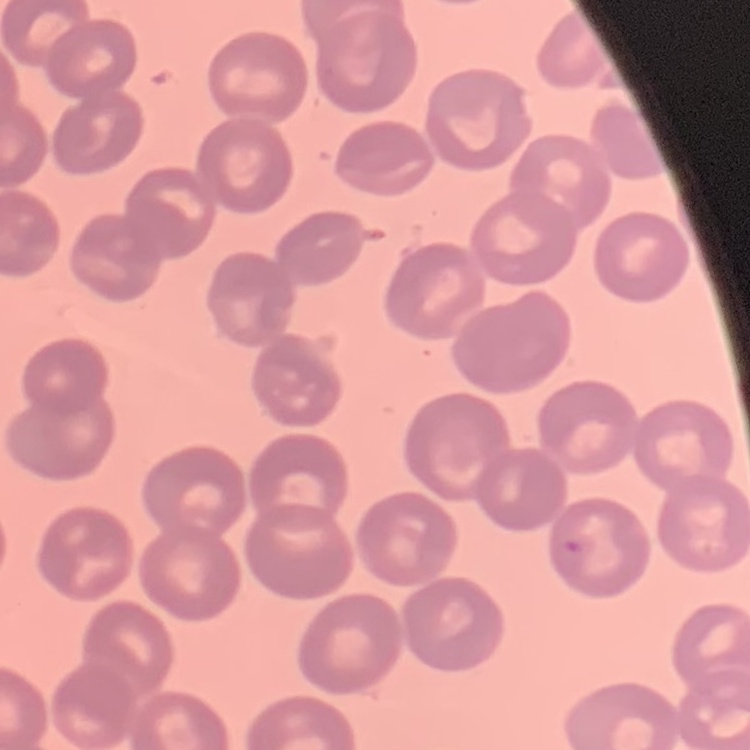
Summary:
  - Red blood cell morphology: no rouleaux formation
  - Image type: one tile cut from a larger photomicrograph
  - Preparation: thin peripheral smear
  - Stain: Field's or Giemsa